Locate and identify every blood parasite.
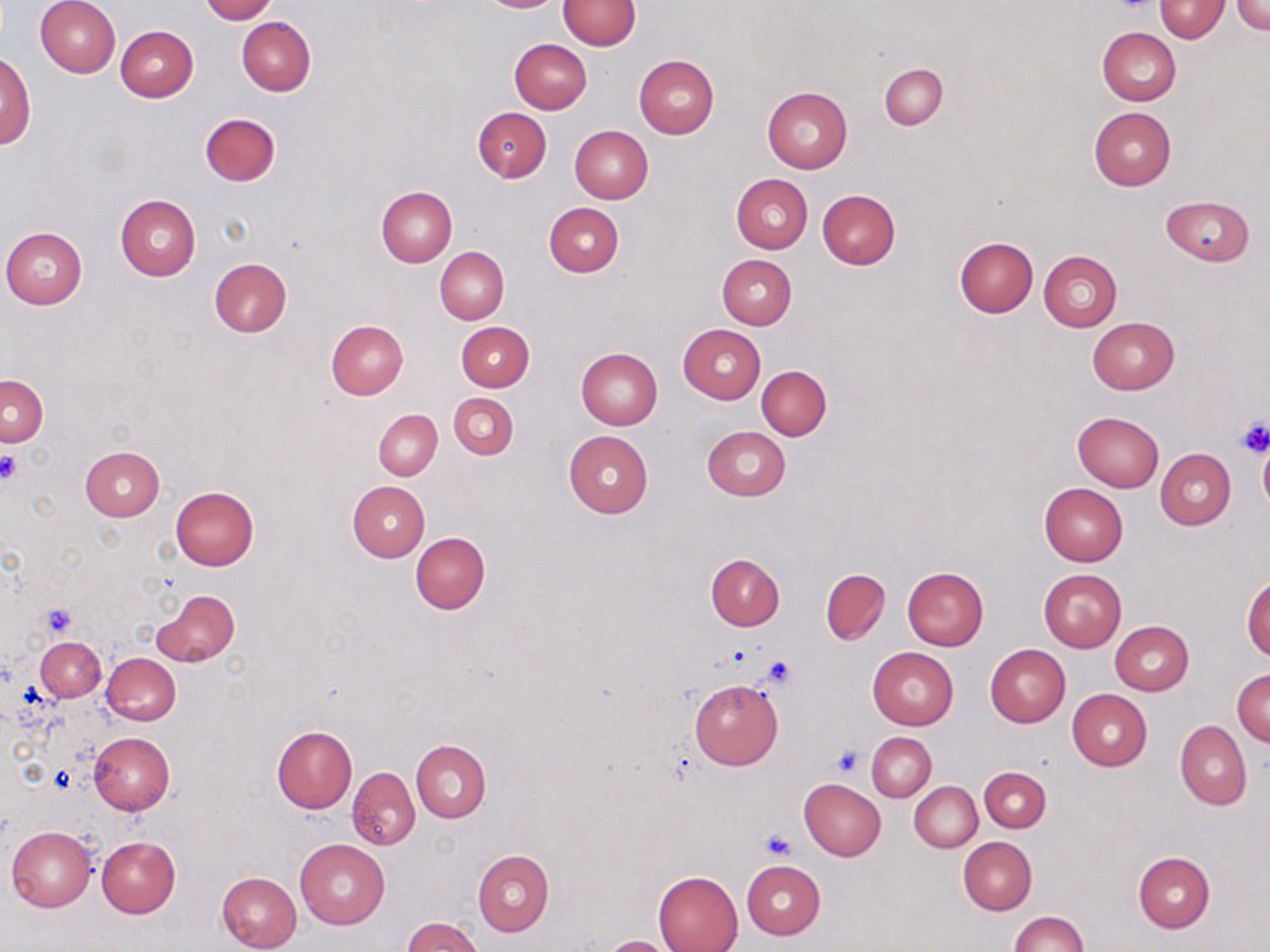

No blood parasites observed.

slide-level diagnosis = no evidence of blood parasites
uninfected red blood cell locations = approximate bounding boxes as (x1, y1, x2, y2) in pixels: (35, 0, 120, 77), (201, 0, 276, 22), (478, 0, 563, 12), (1231, 0, 1270, 34), (558, 1, 639, 50), (1155, 1, 1229, 42), (237, 17, 316, 96), (116, 25, 197, 101), (1097, 27, 1180, 106), (509, 38, 592, 113), (1, 51, 35, 150), (634, 55, 719, 138), (880, 64, 947, 130), (763, 86, 852, 172), (472, 107, 551, 182), (1088, 107, 1175, 190), (200, 113, 280, 186), (570, 125, 653, 203), (731, 173, 813, 253), (377, 186, 457, 266), (817, 189, 900, 269), (114, 194, 201, 280), (1162, 197, 1255, 265), (544, 203, 623, 278), (1, 226, 88, 309), (954, 237, 1037, 317), (435, 246, 509, 323), (1038, 250, 1122, 332), (717, 254, 796, 329), (209, 258, 291, 338), (1087, 316, 1179, 395), (326, 320, 409, 399), (456, 321, 535, 392), (678, 324, 765, 404), (575, 347, 663, 430), (757, 366, 831, 440), (1, 374, 48, 446), (448, 392, 518, 460), (374, 409, 442, 480), (1072, 410, 1164, 492), (702, 427, 791, 500), (563, 430, 652, 518), (1258, 441, 1270, 516), (80, 446, 164, 521), (1155, 448, 1235, 529), (347, 481, 429, 562), (1039, 482, 1127, 566), (170, 485, 259, 571), (411, 533, 490, 615), (705, 554, 784, 631), (902, 566, 989, 649), (821, 569, 890, 645), (1038, 569, 1127, 652), (1243, 574, 1270, 661), (152, 590, 239, 667), (1109, 620, 1194, 695), (36, 637, 105, 702), (985, 645, 1070, 727), (868, 647, 958, 729), (101, 653, 180, 725), (1232, 667, 1270, 746), (689, 679, 783, 770), (1067, 689, 1152, 770), (1176, 721, 1251, 811), (272, 726, 356, 813), (88, 731, 174, 815), (867, 732, 936, 801), (411, 739, 490, 822), (979, 767, 1050, 833), (348, 768, 420, 850), (911, 777, 1048, 842), (799, 779, 886, 861), (910, 782, 982, 852), (7, 826, 97, 912), (97, 836, 179, 917), (957, 838, 1036, 915), (295, 839, 391, 929), (473, 850, 553, 936), (1132, 852, 1214, 933), (741, 860, 825, 939), (216, 871, 302, 952), (654, 871, 743, 952), (1010, 911, 1086, 952), (403, 918, 483, 952), (599, 935, 678, 952)
preparation = thin blood smear
image size = 1270×952 pixels
stain = May-Grünwald-Giemsa
field of view = single
modality = optical microscopy
magnification = 1000x
platelet locations = approximate bounding boxes as (x1, y1, x2, y2) in pixels: (1111, 0, 1157, 14), (1234, 417, 1270, 459), (0, 452, 22, 485), (41, 604, 77, 639), (757, 653, 799, 690), (831, 746, 862, 776), (760, 830, 798, 859)